Describe the morphology of the red blood cells.
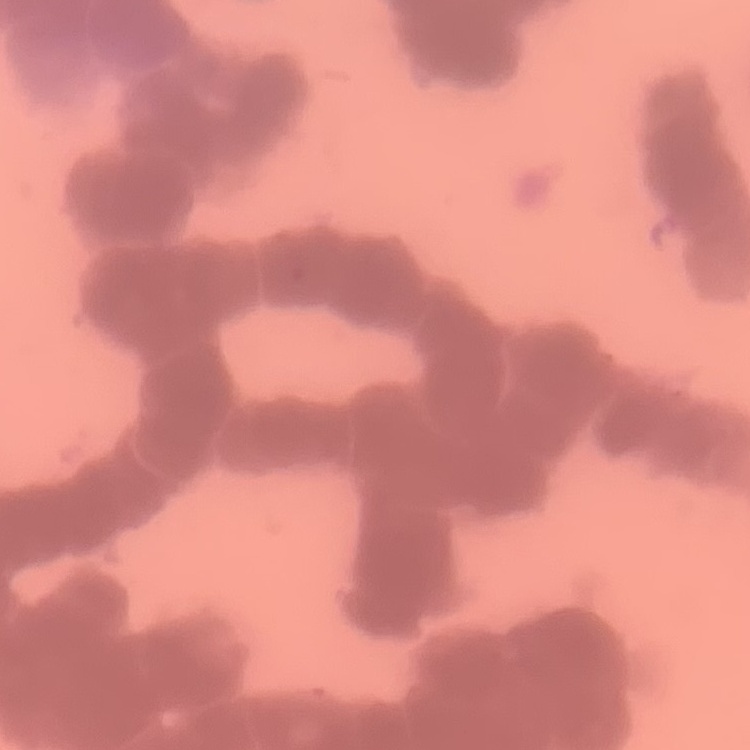

They show rouleaux formation.

Thin peripheral smear. Field's or Giemsa stain. Square crop of a larger photomicrograph.